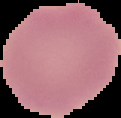

Summary:
  - Preparation: thin blood smear
  - Image size: 121×118 pixels
  - Image type: segmented cell region on a black background
  - Result: no Plasmodium parasites seen